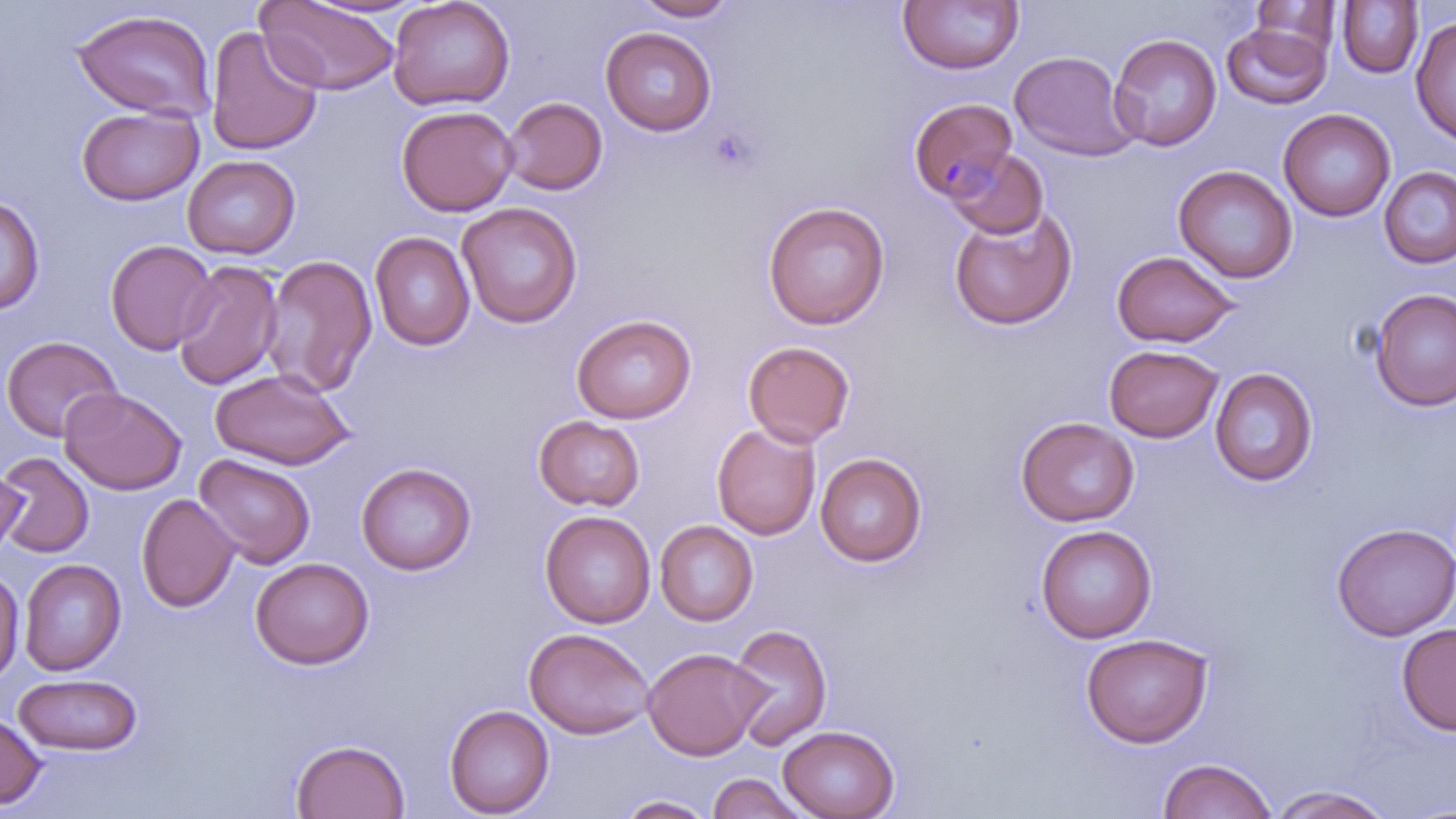
{
  "slide_level_diagnosis": "Plasmodium malariae",
  "stain": "May-Grünwald-Giemsa",
  "magnification": "1000x",
  "platelet_locations": "approximate bounding boxes as (x1,y1)-(x2,y2) corner pairs in pixels: (706,125)-(762,176)",
  "field_of_view": "single",
  "preparation": "thin blood film",
  "modality": "optical microscopy",
  "plasmodium_malariae_infected_red_blood_cell_locations": "approximate bounding boxes as (x1,y1)-(x2,y2) corner pairs in pixels: (908,97)-(1018,202)",
  "image_size": "1456×819 pixels",
  "uninfected_red_blood_cell_locations": "approximate bounding boxes as (x1,y1)-(x2,y2) corner pairs in pixels: (388,0)-(515,112), (632,0)-(740,21), (897,0)-(1024,76), (257,1)-(400,95), (1250,1)-(1341,60), (1337,1)-(1423,79), (71,9)-(218,122), (1410,15)-(1456,145), (1222,23)-(1331,109), (206,25)-(324,156), (600,26)-(717,136), (1108,34)-(1222,151), (1009,50)-(1136,161), (502,97)-(607,195), (76,105)-(203,206), (395,105)-(518,216), (1278,108)-(1395,222), (945,149)-(1048,239), (182,154)-(300,259), (1173,165)-(1297,283), (1378,166)-(1456,269), (0,194)-(44,315), (762,201)-(890,330), (456,202)-(582,328), (949,207)-(1077,330), (370,231)-(475,351), (105,239)-(218,356), (1111,251)-(1240,348), (261,254)-(377,397), (172,259)-(284,391), (1369,289)-(1456,411), (571,314)-(696,424), (1,335)-(122,442), (742,340)-(855,447), (1104,344)-(1223,443), (1209,367)-(1318,487), (209,368)-(355,469), (60,387)-(187,495), (533,415)-(646,512), (1015,416)-(1139,526), (712,423)-(821,540), (0,452)-(94,558), (815,452)-(927,567), (194,454)-(316,569), (356,462)-(476,575), (0,464)-(26,564), (135,493)-(239,613), (540,510)-(655,628), (655,520)-(758,626), (1331,522)-(1456,641), (1034,525)-(1157,643), (250,557)-(374,670), (19,558)-(126,676), (0,568)-(24,686), (1396,622)-(1456,735), (727,623)-(832,750), (524,627)-(655,739), (1080,632)-(1213,748), (642,647)-(769,760), (13,673)-(143,756), (444,704)-(554,817), (0,710)-(46,810), (778,725)-(899,819), (290,738)-(410,819), (1157,757)-(1277,819), (706,773)-(812,819), (1267,785)-(1396,818), (615,794)-(718,818)"
}